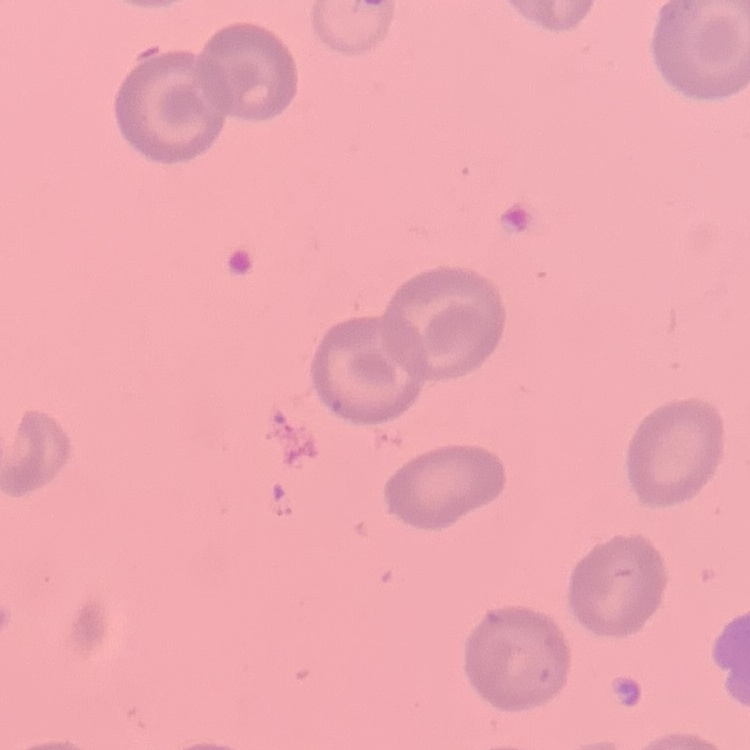 The red blood cells show no rouleaux formation. Thin peripheral smear. Field's or Giemsa stain. One tile cut from a larger photomicrograph.